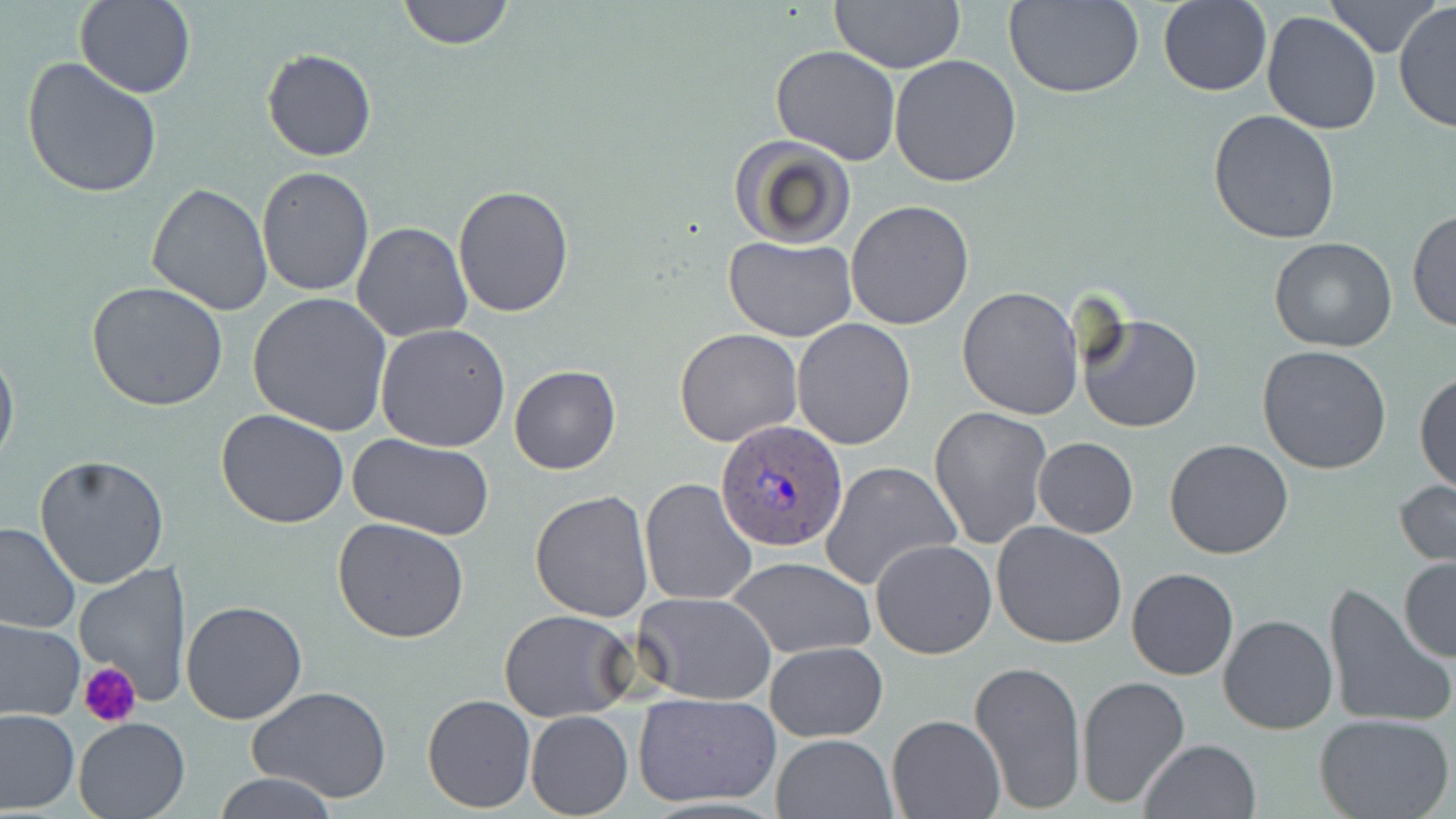

Summary:
  - Coordinate format: approximate bounding boxes as named x1/y1/x2/y2 corners in pixels
  - Platelet locations: (x1=80, y1=663, x2=139, y2=731)
  - Plasmodium ovale-infected red blood cell locations: (x1=716, y1=420, x2=848, y2=550)
  - Uninfected red blood cell locations: (x1=396, y1=0, x2=513, y2=49), (x1=828, y1=0, x2=968, y2=74), (x1=74, y1=1, x2=196, y2=99), (x1=1005, y1=1, x2=1145, y2=98), (x1=1158, y1=1, x2=1271, y2=97), (x1=1321, y1=1, x2=1437, y2=57), (x1=1394, y1=1, x2=1456, y2=134), (x1=1261, y1=10, x2=1381, y2=134), (x1=771, y1=45, x2=902, y2=165), (x1=262, y1=48, x2=377, y2=162), (x1=889, y1=55, x2=1023, y2=189), (x1=21, y1=57, x2=163, y2=200), (x1=1208, y1=110, x2=1342, y2=245), (x1=728, y1=134, x2=858, y2=250), (x1=257, y1=167, x2=374, y2=297), (x1=147, y1=183, x2=273, y2=317), (x1=453, y1=185, x2=576, y2=319), (x1=846, y1=200, x2=974, y2=329), (x1=1408, y1=210, x2=1455, y2=334), (x1=351, y1=222, x2=472, y2=341), (x1=722, y1=235, x2=858, y2=342), (x1=1269, y1=236, x2=1398, y2=353), (x1=86, y1=282, x2=228, y2=411), (x1=957, y1=286, x2=1084, y2=420), (x1=248, y1=291, x2=393, y2=436), (x1=1074, y1=312, x2=1203, y2=433), (x1=790, y1=318, x2=916, y2=449), (x1=375, y1=323, x2=511, y2=450), (x1=674, y1=328, x2=802, y2=446), (x1=0, y1=344, x2=19, y2=470), (x1=1258, y1=345, x2=1392, y2=474), (x1=509, y1=365, x2=622, y2=475), (x1=1414, y1=370, x2=1456, y2=493), (x1=929, y1=405, x2=1052, y2=548), (x1=216, y1=409, x2=350, y2=530), (x1=349, y1=435, x2=493, y2=540), (x1=1033, y1=436, x2=1139, y2=538), (x1=1164, y1=438, x2=1294, y2=558), (x1=34, y1=457, x2=169, y2=590), (x1=820, y1=461, x2=963, y2=593), (x1=641, y1=477, x2=759, y2=608), (x1=1394, y1=478, x2=1456, y2=567), (x1=530, y1=490, x2=654, y2=622), (x1=332, y1=517, x2=470, y2=644), (x1=0, y1=520, x2=81, y2=633), (x1=992, y1=521, x2=1128, y2=649), (x1=870, y1=539, x2=998, y2=659), (x1=727, y1=555, x2=877, y2=660), (x1=1398, y1=557, x2=1455, y2=664), (x1=74, y1=562, x2=193, y2=707), (x1=1126, y1=568, x2=1238, y2=680), (x1=1323, y1=582, x2=1452, y2=730), (x1=632, y1=593, x2=776, y2=706), (x1=181, y1=599, x2=308, y2=724), (x1=498, y1=609, x2=635, y2=722), (x1=1218, y1=612, x2=1337, y2=735), (x1=1, y1=618, x2=85, y2=720), (x1=765, y1=641, x2=888, y2=742), (x1=969, y1=660, x2=1086, y2=816), (x1=1077, y1=675, x2=1190, y2=810), (x1=247, y1=686, x2=392, y2=804), (x1=422, y1=693, x2=535, y2=811), (x1=633, y1=693, x2=781, y2=808), (x1=0, y1=710, x2=78, y2=813), (x1=525, y1=711, x2=634, y2=818), (x1=1314, y1=714, x2=1456, y2=819), (x1=887, y1=715, x2=1004, y2=819), (x1=73, y1=717, x2=192, y2=818), (x1=772, y1=733, x2=896, y2=819), (x1=1139, y1=738, x2=1259, y2=819), (x1=214, y1=772, x2=340, y2=818)
  - Slide-level diagnosis: Plasmodium ovale
  - Modality: light microscopy
  - Preparation: thin blood smear
  - Field of view: single
  - Image size: 1456×819 pixels
  - Magnification: 1000x
  - Stain: May-Grünwald-Giemsa